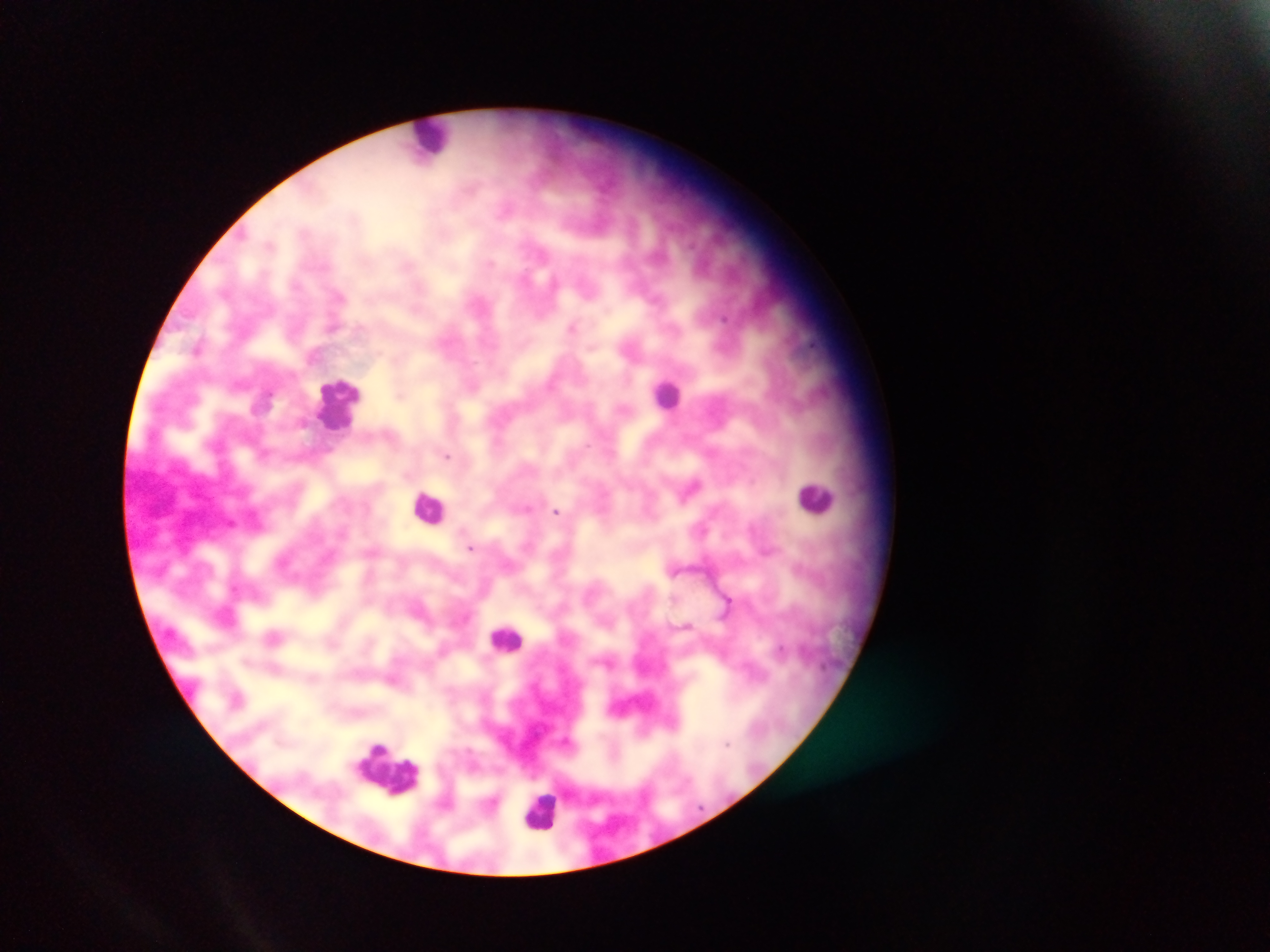
field_of_view: single
country: Ghana
leukocyte_locations: 'approximate centers as [x, y] in pixels: [431, 138], [667, 394], [339, 404], [815, 497], [430, 507], [507, 638], [387, 767], [541, 811]'
capture: mobile-phone photograph through a microscope
image_size: 1270×952 pixels
malaria_parasite_locations: 'approximate centers as [x, y] in pixels: [573, 327], [198, 349], [401, 395], [448, 455], [691, 486], [527, 508], [557, 511], [471, 547], [727, 603], [727, 742]'
preparation: thick blood film